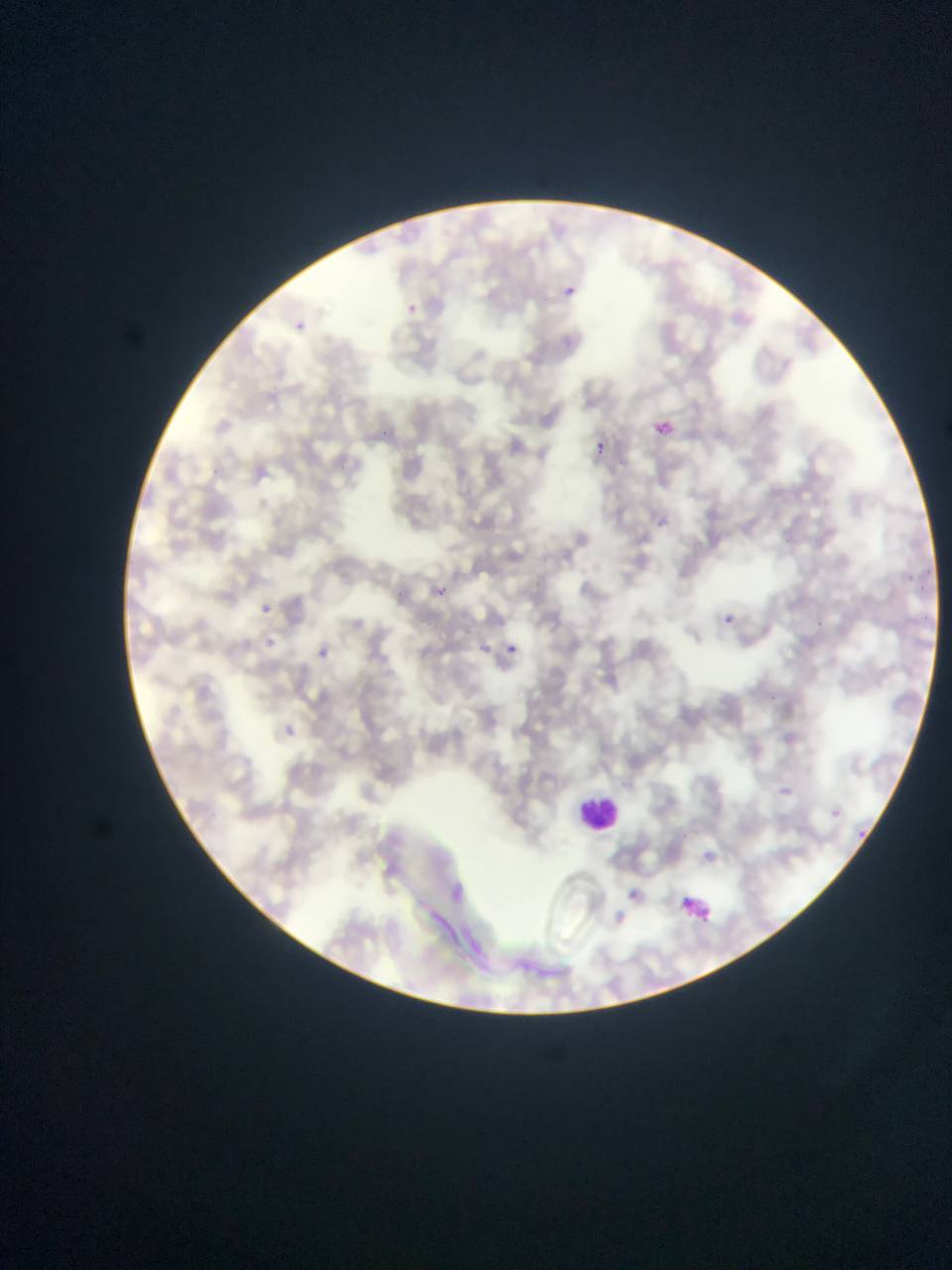
image size = 952×1270 pixels
malaria parasite locations = approximate bounding boxes as {left, top, right, bottom} in pixels: {565, 268, 600, 319}, {393, 294, 429, 334}, {294, 321, 306, 331}, {650, 403, 667, 441}, {590, 443, 615, 471}, {643, 494, 673, 530}, {433, 577, 473, 627}, {248, 592, 286, 620}, {707, 599, 742, 630}, {261, 628, 286, 656}, {476, 630, 494, 661}, {306, 638, 357, 683}, {497, 640, 525, 661}, {266, 719, 319, 757}, {774, 777, 795, 800}, {826, 795, 856, 821}, {853, 809, 870, 845}, {696, 840, 722, 873}, {450, 875, 483, 915}, {612, 876, 655, 909}, {597, 913, 628, 946}
preparation = thin blood smear
field of view = single
capture = mobile-phone photograph through a microscope
leukocyte locations = approximate bounding boxes as {left, top, right, bottom} in pixels: {562, 781, 648, 831}
country = Ghana